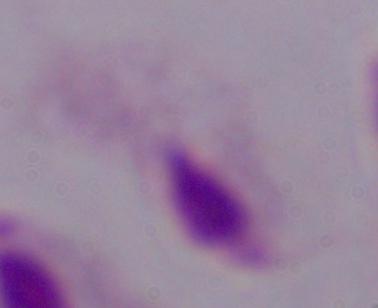 Micrograph. Captured at 1000x magnification. A trichomonad is seen.